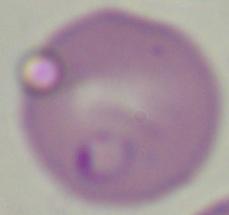 Captured at 1000x magnification. Photomicrograph. A Babesia parasite is shown.